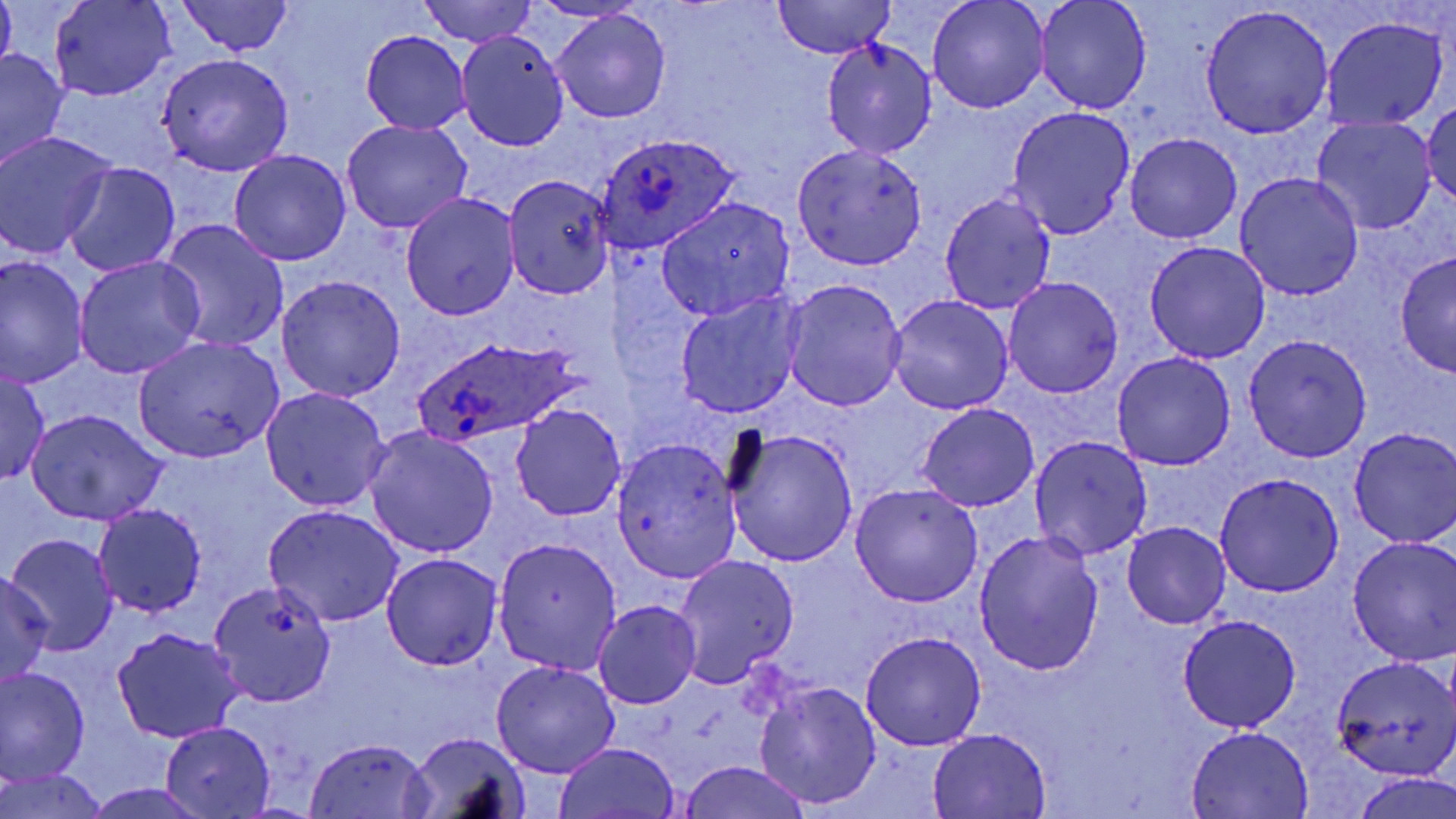
Summary:
  - Coordinate format: approximate bounding boxes as (x1, y1, x2, y2) in pixels
  - Uninfected red blood cell locations: (1, 0, 17, 75), (49, 0, 177, 100), (416, 0, 536, 48), (926, 0, 1050, 113), (1035, 0, 1151, 115), (173, 1, 295, 57), (775, 1, 897, 58), (1199, 5, 1335, 139), (550, 9, 672, 124), (1323, 17, 1447, 131), (457, 30, 568, 149), (359, 32, 471, 133), (821, 38, 936, 161), (0, 48, 69, 172), (155, 53, 293, 176), (1423, 99, 1455, 208), (1006, 107, 1135, 239), (1312, 116, 1436, 235), (341, 119, 473, 235), (0, 131, 117, 258), (1125, 133, 1242, 244), (791, 142, 929, 269), (230, 149, 351, 267), (63, 163, 180, 278), (1234, 170, 1367, 300), (501, 173, 616, 299), (400, 191, 520, 320), (938, 192, 1057, 314), (657, 197, 795, 322), (158, 219, 290, 353), (1143, 241, 1272, 363), (1393, 248, 1456, 379), (0, 256, 87, 390), (74, 256, 205, 379), (275, 274, 406, 401), (1002, 277, 1124, 399), (782, 279, 906, 413), (674, 292, 806, 419), (887, 294, 1013, 415), (1244, 333, 1371, 461), (134, 336, 284, 461), (1111, 352, 1236, 471), (0, 368, 49, 486), (261, 387, 391, 511), (511, 401, 628, 521), (916, 402, 1040, 511), (27, 410, 167, 526), (364, 426, 498, 558), (724, 426, 858, 567), (1348, 426, 1456, 547), (1030, 433, 1152, 561), (611, 435, 742, 583), (1214, 473, 1344, 598), (850, 483, 984, 608), (95, 504, 207, 617), (263, 504, 406, 627), (1123, 523, 1231, 629), (973, 529, 1103, 677), (6, 534, 119, 657), (1347, 535, 1455, 665), (492, 538, 623, 673), (380, 553, 501, 671), (671, 556, 798, 688), (0, 571, 52, 687), (207, 580, 335, 706), (593, 601, 701, 708), (1177, 615, 1302, 733), (113, 628, 245, 744), (861, 632, 987, 751), (1329, 656, 1456, 780), (490, 661, 621, 779), (1, 668, 88, 786), (756, 680, 879, 807), (159, 721, 276, 818), (1184, 725, 1315, 817), (928, 727, 1052, 818), (405, 732, 529, 817), (304, 737, 434, 818), (554, 742, 682, 818), (677, 761, 814, 819), (1, 770, 111, 819), (1352, 772, 1456, 819), (85, 783, 209, 818)
  - Plasmodium ovale-infected red blood cell locations: (596, 131, 741, 255), (418, 339, 580, 445)
  - Slide-level diagnosis: Plasmodium ovale
  - Preparation: thin blood film
  - Image size: 1456×819 pixels
  - Magnification: 1000x
  - Stain: May-Grünwald-Giemsa
  - Field of view: one of a larger specimen
  - Modality: light microscopy